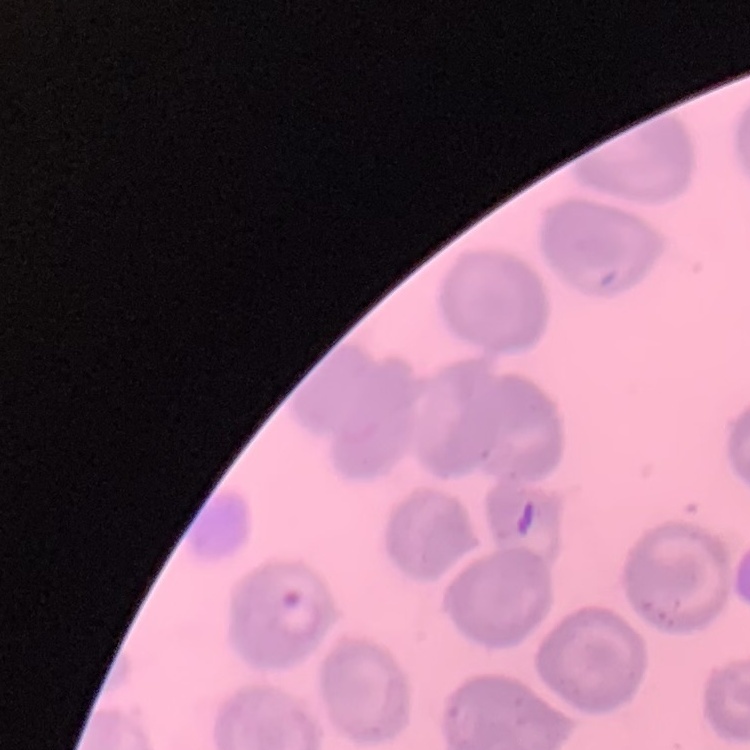

The erythrocytes show no rouleaux formation. One tile cut from a larger photomicrograph. Thin blood film. Stained with either Field's or Giemsa.